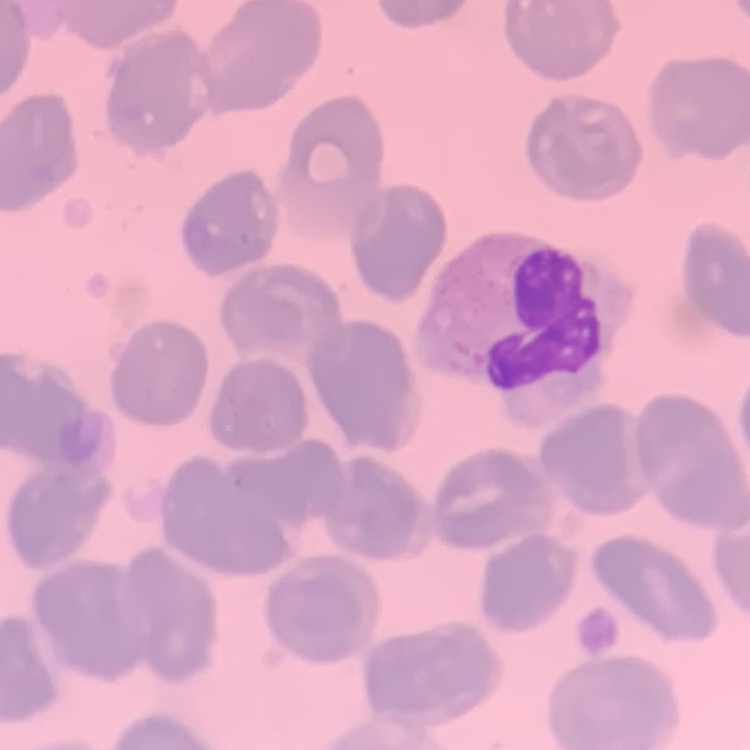

Summary:
  - Erythrocyte morphology: no rouleaux formation
  - Preparation: thin blood film
  - Stain: Field's or Giemsa
  - Image type: one tile cut from a larger photomicrograph